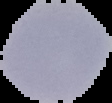
{
  "result": "negative for Plasmodium parasites",
  "image_type": "segmented cell region with the area outside set to black",
  "image_size": "112×103 pixels",
  "preparation": "thin blood film"
}